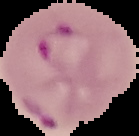
Image is 139×136 pixels. Malaria status: parasitized. From a thin blood film. Segmented cell region on a black background.